Classify this cell by malaria status.
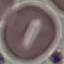

It is uninfected.

Giemsa stain. Automatically extracted cell patch, resized to 64 × 64 pixels. Acquired by smartphone through the microscope eyepiece. Thin smear of blood.